Classify this cell by malaria status.
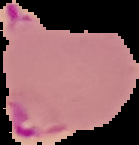
Parasitized.

image size = 139×145 pixels
image type = cell region segmented out of the field of view; surrounding area masked to black
preparation = thin blood film